Name the parasite shown.
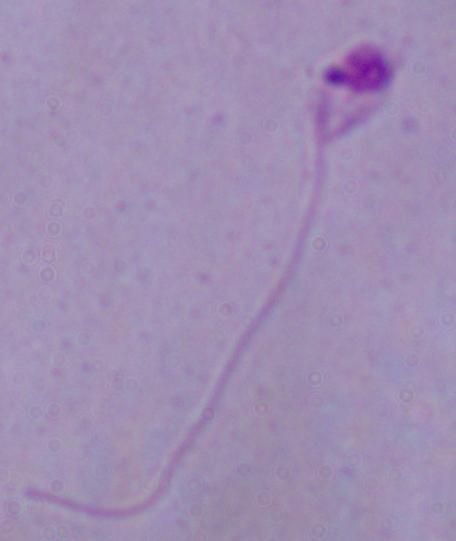
Leishmania.

modality: micrograph
magnification: 1000x